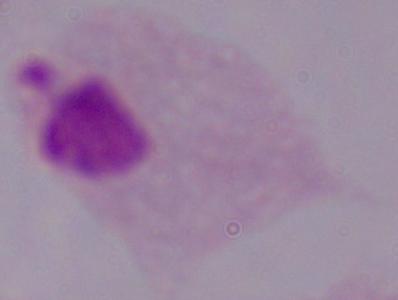
Summary:
  - Modality: micrograph
  - Magnification: 1000x
  - Identification: trichomonad